Report the malaria status of this cell.
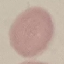
Uninfected.

Giemsa-stained preparation. Thin smear of blood. Cell patch, automatically extracted from a larger field of view and resized to 64 × 64 pixels. Acquired by smartphone through the microscope eyepiece.